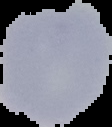 The area outside the segmented cell region is set to black. From a thin blood smear. Malaria status: uninfected. Image is 112×127 pixels.